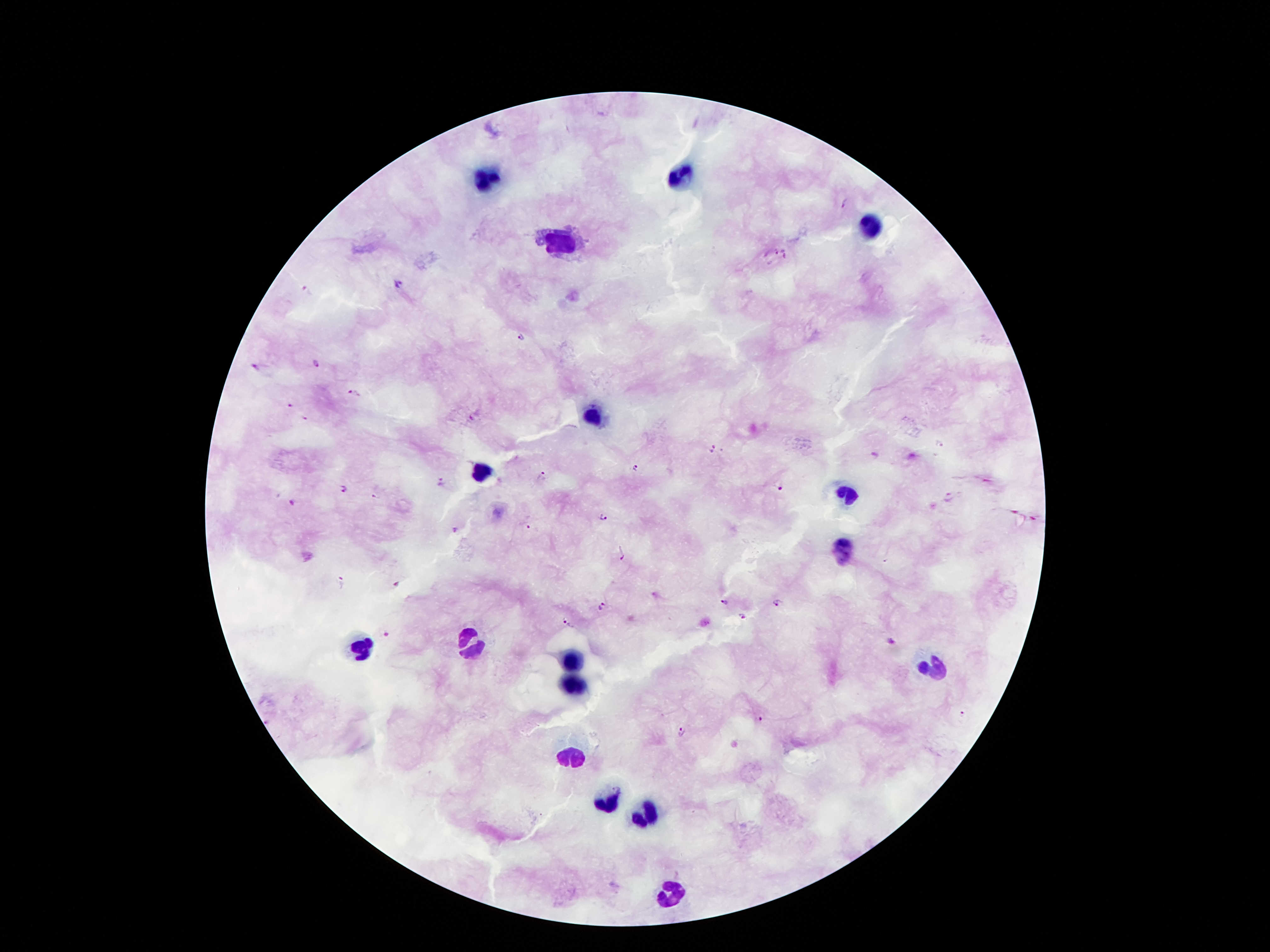

{
  "malaria_parasite_locations": "approximate centers as [x, y] in pixels: [845, 203], [774, 251], [785, 253], [398, 283], [307, 291], [521, 337], [315, 364], [255, 366], [355, 393], [290, 406], [473, 417], [304, 419], [939, 445], [713, 449], [876, 454], [636, 468], [541, 476], [441, 483], [779, 485], [343, 491], [376, 495], [949, 498], [293, 502], [602, 518], [529, 528], [452, 531], [621, 554], [341, 583], [398, 584], [724, 603], [778, 603], [601, 606], [741, 617], [567, 622], [387, 634], [892, 642], [963, 714], [762, 718], [680, 731]",
  "capture": "smartphone camera through the microscope eyepiece",
  "magnification": "100x",
  "patient_malaria_status": "positive for Plasmodium falciparum",
  "leukocyte_locations": "approximate centers as [x, y] in pixels: [679, 176], [488, 178], [870, 224], [561, 244], [593, 414], [481, 474], [845, 496], [844, 548], [473, 644], [360, 650], [572, 662], [939, 669], [574, 684], [572, 760], [605, 802], [645, 818], [672, 894]",
  "image_size": "1270×952 pixels",
  "field_of_view": "one from this slide",
  "preparation": "thick blood smear",
  "stain": "Giemsa"
}